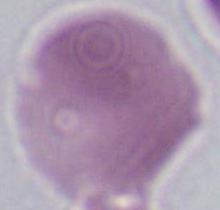

Summary:
  - Identification: erythrocyte
  - Modality: photomicrograph
  - Magnification: 1000x